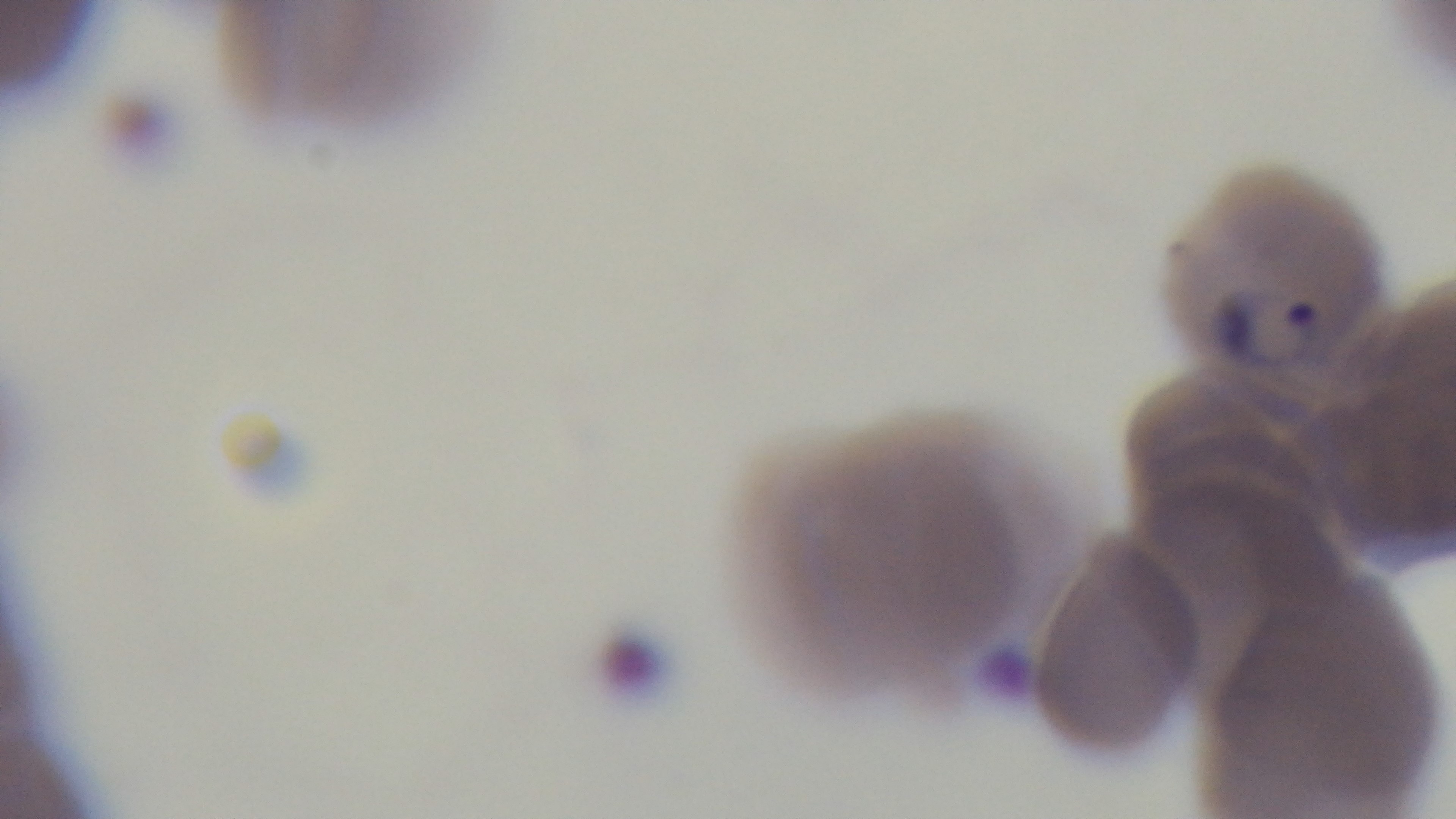

Mounted 4K digital camera. One field from the slide. Preparation: thin. 100x oil-immersion objective. Giemsa-stained. Light microscopy. Malaria status: positive.